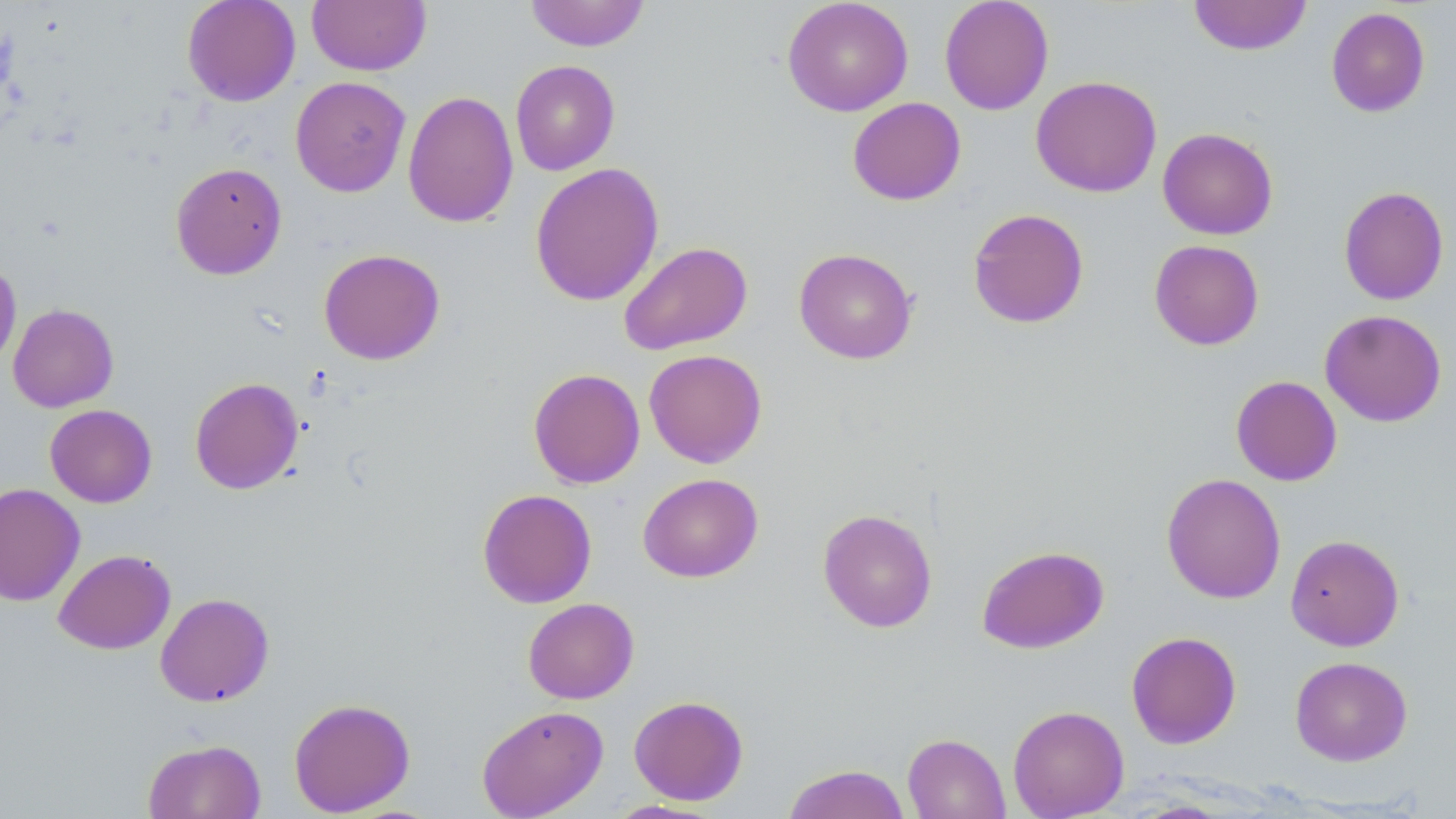

Approximate bounding boxes as (x1,y1)-(x2,y2) corner pairs in pixels. Uninfected red blood cell locations: (182,0)-(301,106), (306,0)-(431,76), (524,0)-(651,52), (782,0)-(913,116), (939,0)-(1054,115), (1188,0)-(1311,56), (1326,6)-(1431,117), (510,60)-(620,175), (1031,75)-(1162,198), (290,76)-(411,197), (403,90)-(519,229), (847,97)-(966,205), (1157,127)-(1278,240), (170,162)-(287,280), (530,162)-(664,306), (1338,185)-(1450,306), (967,208)-(1089,329), (1149,239)-(1265,350), (618,241)-(753,356), (794,247)-(918,364), (318,248)-(445,365), (0,259)-(21,373), (8,303)-(119,412), (1319,309)-(1447,427), (644,349)-(767,468), (528,368)-(645,489), (1230,375)-(1342,486), (189,376)-(304,495), (45,404)-(157,507), (637,473)-(763,582), (1161,473)-(1286,604), (0,483)-(85,606), (477,488)-(597,608), (818,508)-(938,633), (1286,534)-(1404,651), (976,545)-(1109,653), (53,549)-(175,654), (155,592)-(274,707), (523,598)-(639,704), (1126,631)-(1242,749), (1290,656)-(1413,766), (629,695)-(748,805), (288,698)-(416,816), (477,705)-(609,819), (1007,705)-(1129,818), (902,733)-(1011,819), (143,738)-(266,819), (782,763)-(910,819), (603,799)-(726,818). Slide-level diagnosis: no evidence of blood parasites. Optical microscopy. Thin blood smear. 1000x magnification. One field of a larger specimen. Image is 1456×819 pixels. May-Grünwald-Giemsa-stained preparation.